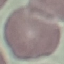
Malaria status: uninfected. Giemsa-stained preparation. Thin blood film. Automatically extracted cell patch, resized to 64 × 64 pixels. Photographed with a smartphone camera at the microscope eyepiece.